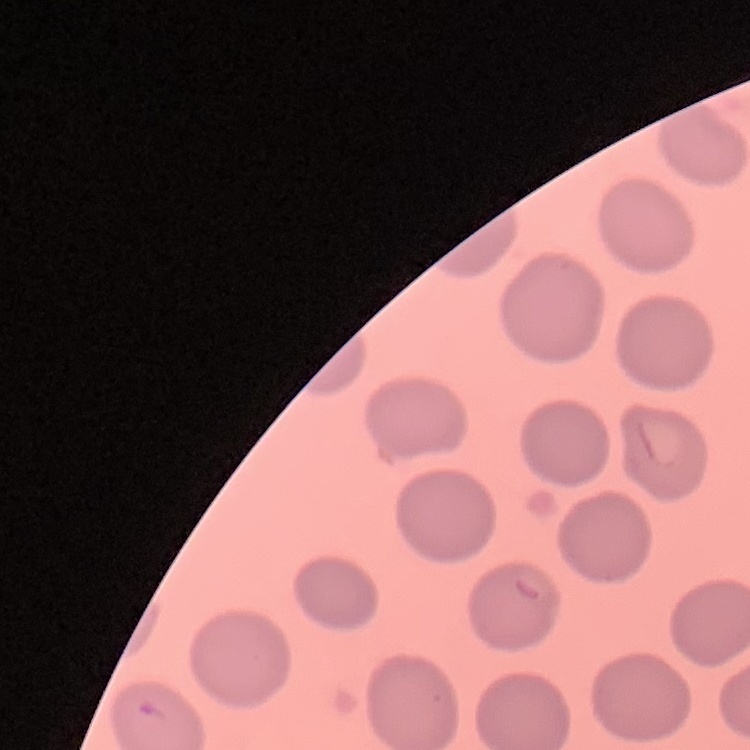

Summary:
  - Erythrocyte morphology: no rouleaux formation
  - Image type: square crop of a larger photomicrograph
  - Stain: Field's or Giemsa
  - Preparation: thin blood smear